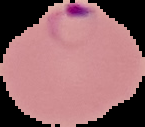 Image is 145×127 pixels. From a thin blood film. Malaria status: parasitized. Cell region segmented out of the field of view; the surrounding area is masked to black.